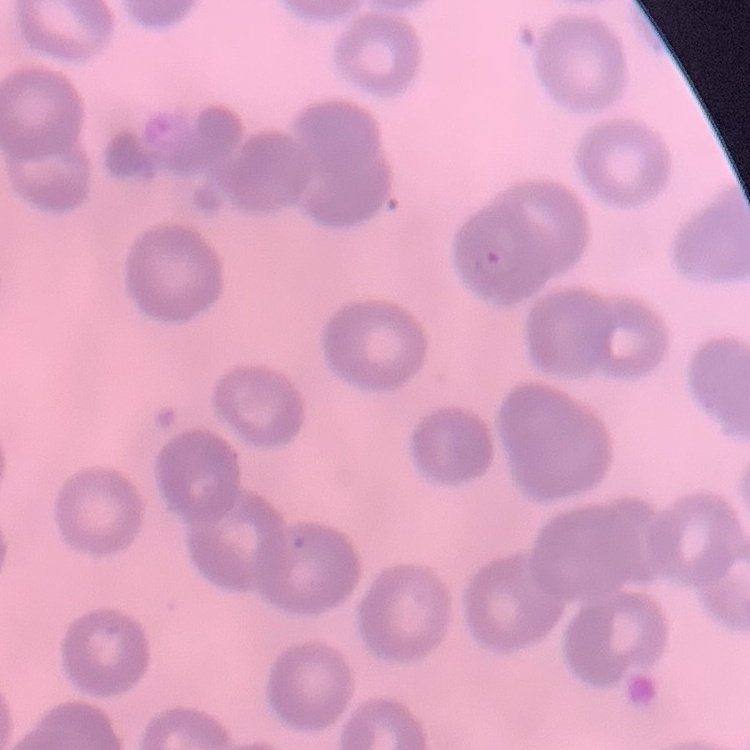
Summary:
  - Erythrocyte morphology: no rouleaux formation
  - Preparation: thin blood film
  - Image type: square crop of a larger photomicrograph
  - Stain: Field's or Giemsa